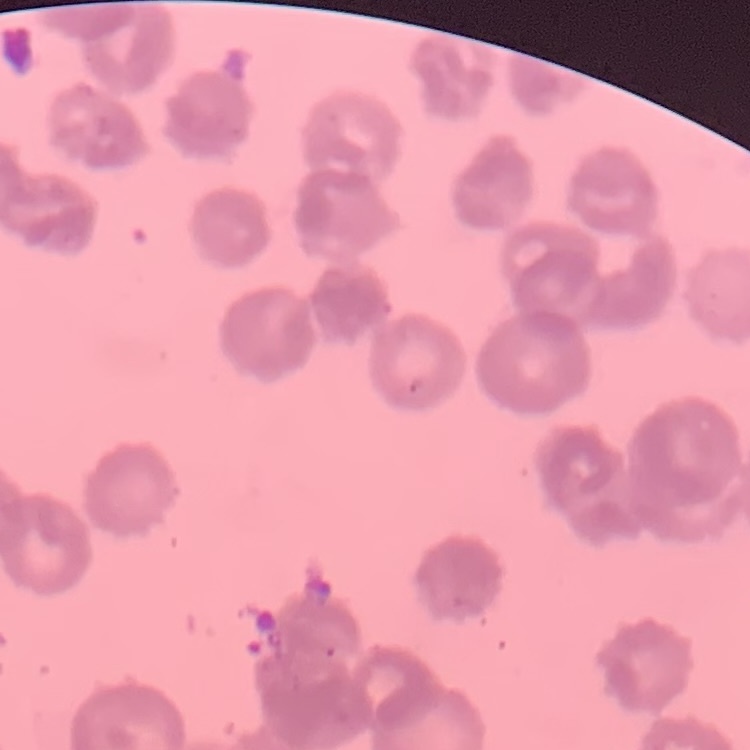
The erythrocytes show rouleaux formation. One tile cut from a larger photomicrograph. Thin blood film. Stained with either Field's or Giemsa.